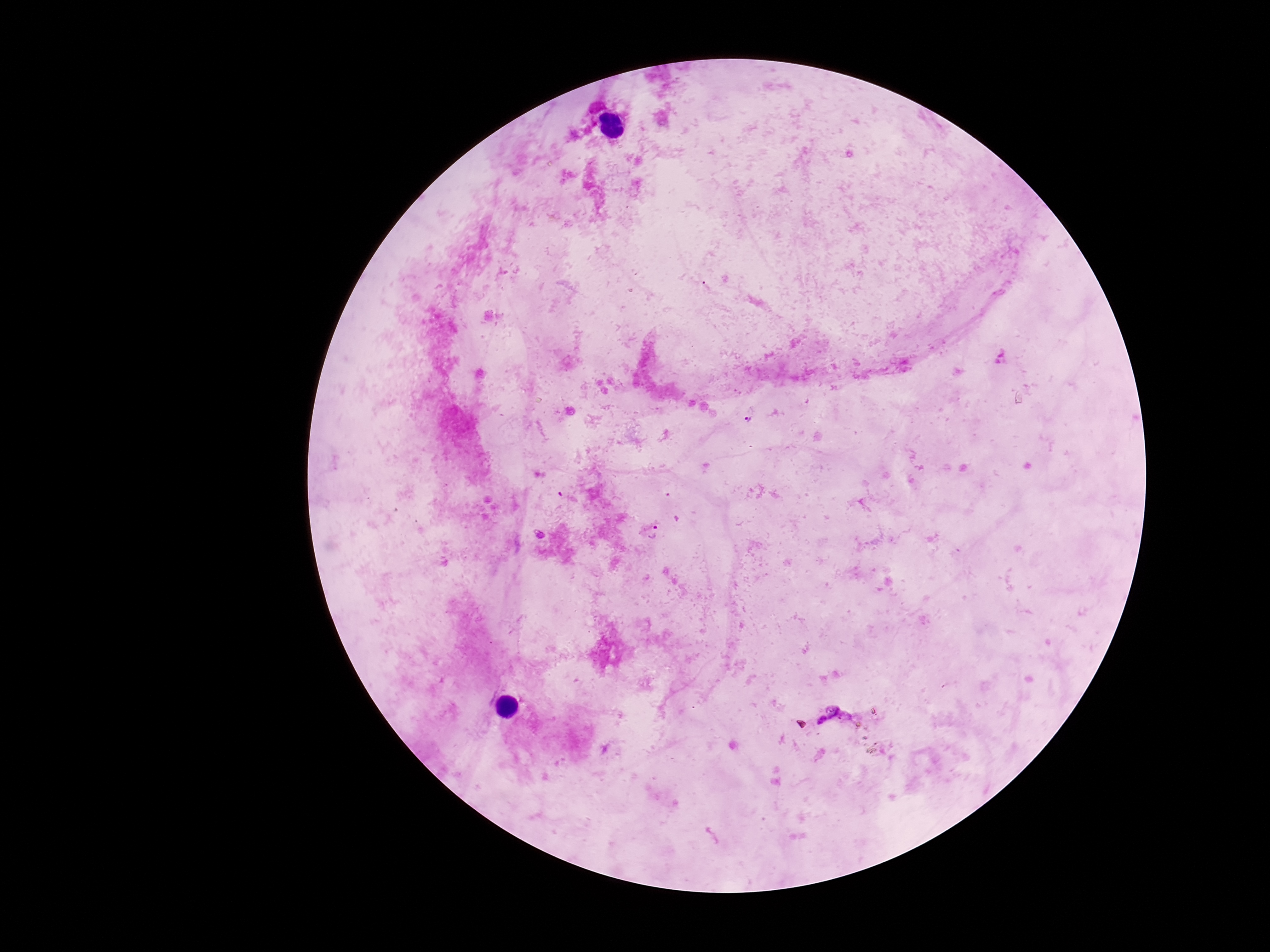

preparation: thick blood film
plasmodium_parasite_locations: 'approximate centers as {x, y} in pixels: {748, 420}, {655, 533}, {834, 712}'
stain: Giemsa
field_of_view: single
capture: smartphone camera through the microscope eyepiece
image_size: 1270×952 pixels
magnification: 100x
patient_malaria_status: infected